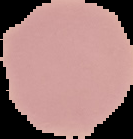

malaria status = uninfected
preparation = thin blood smear
image size = 133×139 pixels
image type = segmented cell region on a black background